Identify the parasite.
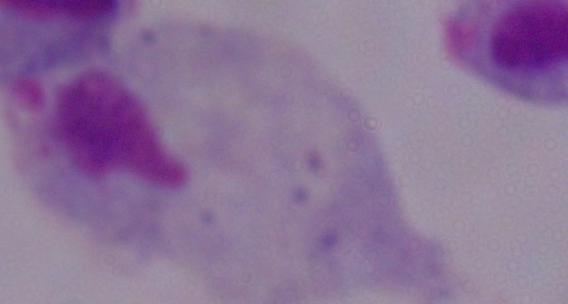
A trichomonad.

{
  "modality": "photomicrograph",
  "magnification": "1000x"
}